Locate every blood parasite and identify its species.
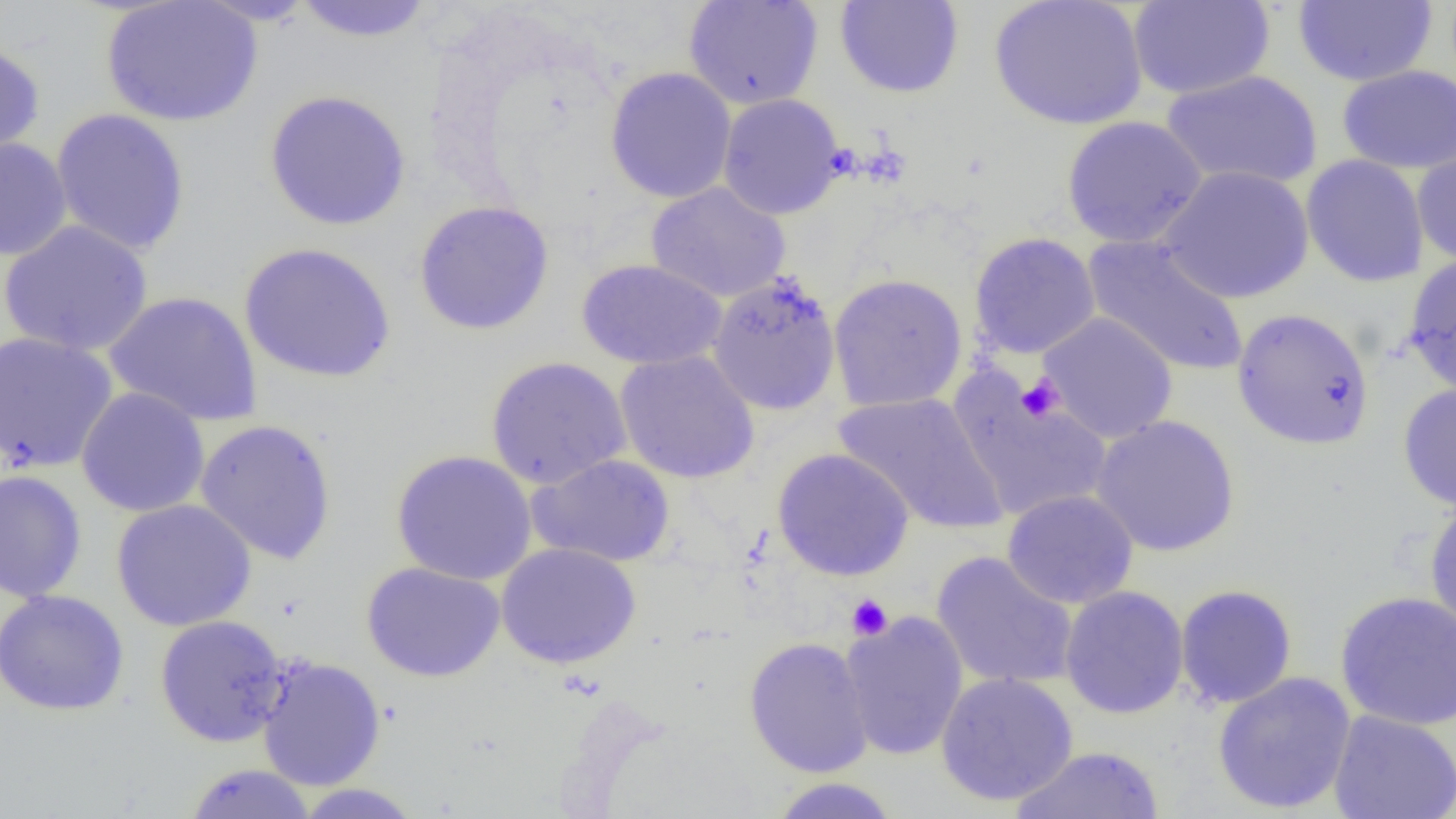
No blood parasites observed.

Approximate bounding boxes as (x1,y1)-(x2,y2) corner pairs in pixels. Platelet locations: (1017,373)-(1065,422), (846,594)-(893,640). Uninfected red blood cell locations: (100,0)-(264,127), (291,0)-(436,42), (683,0)-(823,110), (834,0)-(965,99), (989,0)-(1148,131), (1128,0)-(1275,100), (1293,0)-(1438,87), (0,38)-(46,169), (1336,64)-(1456,174), (604,67)-(737,203), (1161,69)-(1323,191), (264,89)-(412,232), (717,93)-(847,220), (50,108)-(191,256), (1061,115)-(1207,249), (0,136)-(72,262), (1411,143)-(1456,267), (1301,155)-(1430,287), (1157,166)-(1314,304), (645,182)-(791,303), (413,200)-(554,335), (0,220)-(154,357), (969,232)-(1101,359), (1083,235)-(1249,378), (238,242)-(397,384), (1402,254)-(1456,398), (575,258)-(727,370), (707,272)-(841,416), (828,272)-(968,413), (104,291)-(263,427), (1231,307)-(1376,450), (1037,312)-(1178,444), (0,333)-(119,473), (615,350)-(760,484), (485,356)-(632,489), (947,374)-(1114,522), (1397,384)-(1456,511), (76,387)-(210,517), (833,391)-(1009,535), (1090,414)-(1240,557), (194,418)-(338,565), (772,448)-(914,581), (390,450)-(537,586), (526,454)-(675,567), (0,470)-(87,603), (1002,489)-(1139,609), (111,499)-(257,632), (1424,500)-(1456,637), (496,542)-(641,669), (931,551)-(1079,691), (361,561)-(505,683), (1175,584)-(1297,709), (1059,585)-(1189,719), (0,589)-(129,716), (1335,590)-(1456,730), (839,612)-(969,761), (154,615)-(291,747), (744,636)-(874,778), (256,655)-(387,790), (935,671)-(1078,807), (1212,671)-(1357,814), (1328,710)-(1456,819), (1009,744)-(1165,819), (182,763)-(318,819), (767,777)-(902,818), (291,783)-(426,818). Slide-level diagnosis: negative for blood parasites. Single field of view. 1000x magnification. Thin blood film. Optical microscopy. Image is 1456×819 pixels.